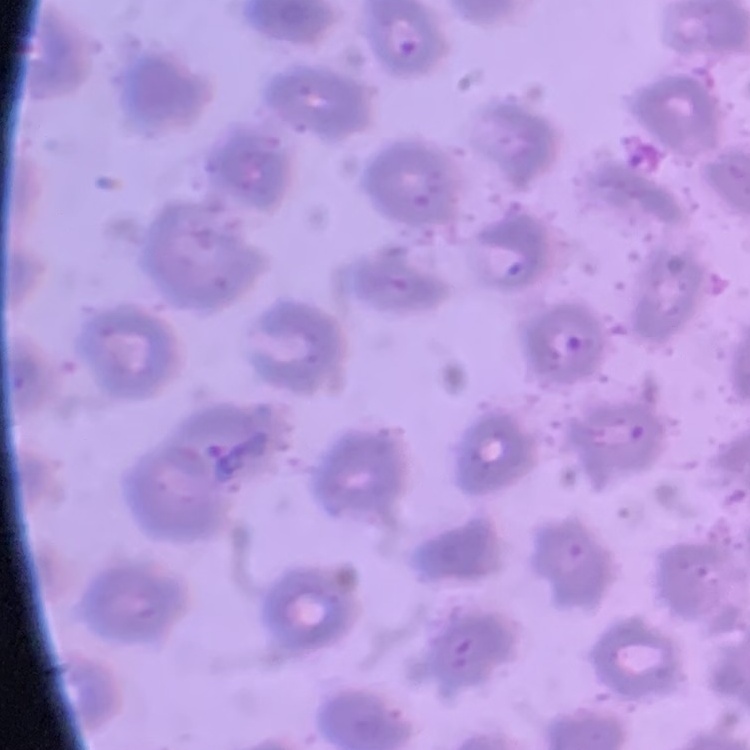
The erythrocytes exhibit no rouleaux formation. Thin blood film. One tile cut from a larger photomicrograph. Field's or Giemsa stain.